State the blood parasite species.
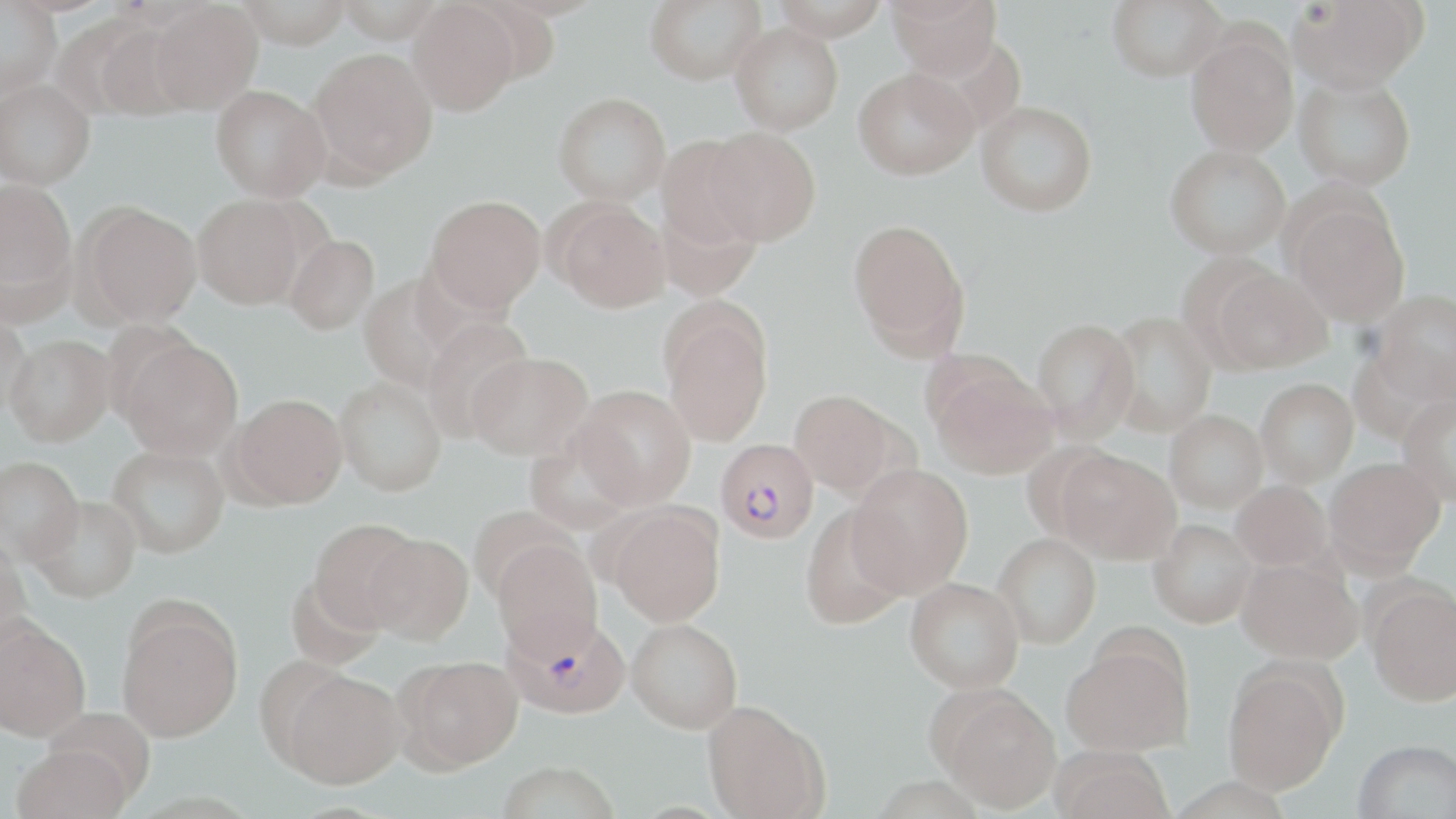

Plasmodium falciparum.

Summary:
  - Coordinate format: approximate bounding boxes as (x1,y1)-(x2,y2) corner pairs in pixels
  - Plasmodium falciparum-infected red blood cell locations: (716,438)-(819,544), (504,611)-(630,717)
  - Uninfected red blood cell locations: (236,0)-(351,48), (334,0)-(446,42), (645,0)-(767,85), (771,0)-(890,40), (886,0)-(1002,79), (1107,0)-(1228,81), (1289,0)-(1427,92), (0,1)-(62,99), (149,1)-(263,114), (408,1)-(521,116), (87,18)-(194,120), (729,21)-(843,135), (1186,32)-(1299,158), (308,47)-(438,183), (852,67)-(978,180), (1294,73)-(1415,191), (0,79)-(96,189), (211,84)-(331,201), (553,91)-(672,205), (976,101)-(1097,216), (703,126)-(821,246), (655,135)-(763,251), (1165,145)-(1291,258), (0,177)-(77,303), (193,194)-(308,309), (424,195)-(546,313), (657,198)-(762,301), (551,199)-(671,312), (1287,200)-(1409,326), (78,202)-(202,327), (847,216)-(970,356), (284,235)-(380,335), (1212,267)-(1331,373), (358,274)-(466,392), (1370,290)-(1456,402), (661,305)-(774,445), (0,306)-(34,418), (1104,311)-(1217,437), (421,316)-(535,441), (1031,317)-(1139,443), (5,335)-(115,446), (118,337)-(244,460), (468,352)-(592,460), (930,364)-(1058,480), (335,377)-(446,496), (1255,378)-(1358,486), (572,384)-(697,508), (788,389)-(900,497), (230,393)-(347,507), (1396,393)-(1456,506), (1165,410)-(1268,513), (523,435)-(638,535), (107,444)-(229,558), (1058,450)-(1180,564), (0,455)-(84,563), (1324,456)-(1445,571), (847,465)-(973,596), (1231,480)-(1332,571), (31,495)-(142,603), (607,505)-(725,627), (799,505)-(910,629), (468,506)-(579,604), (309,519)-(421,632), (1148,519)-(1258,628), (364,532)-(474,644), (992,534)-(1101,649), (0,540)-(32,655), (492,540)-(603,661), (1237,557)-(1362,663), (286,574)-(387,670), (905,577)-(1024,693), (1365,583)-(1455,706), (117,608)-(242,741), (627,618)-(743,733), (0,619)-(91,741), (1062,645)-(1191,755), (398,655)-(524,771), (1222,663)-(1345,794), (281,670)-(406,788), (938,689)-(1061,813), (701,701)-(828,819), (39,707)-(156,802), (1353,739)-(1456,819), (11,744)-(132,819), (1051,748)-(1176,819), (498,761)-(619,819)
  - Magnification: 1000x
  - Preparation: thin blood smear
  - Image size: 1456×819 pixels
  - Field of view: one of a larger specimen
  - Modality: light microscopy
  - Stain: May-Grünwald-Giemsa